Locate every malaria parasite.
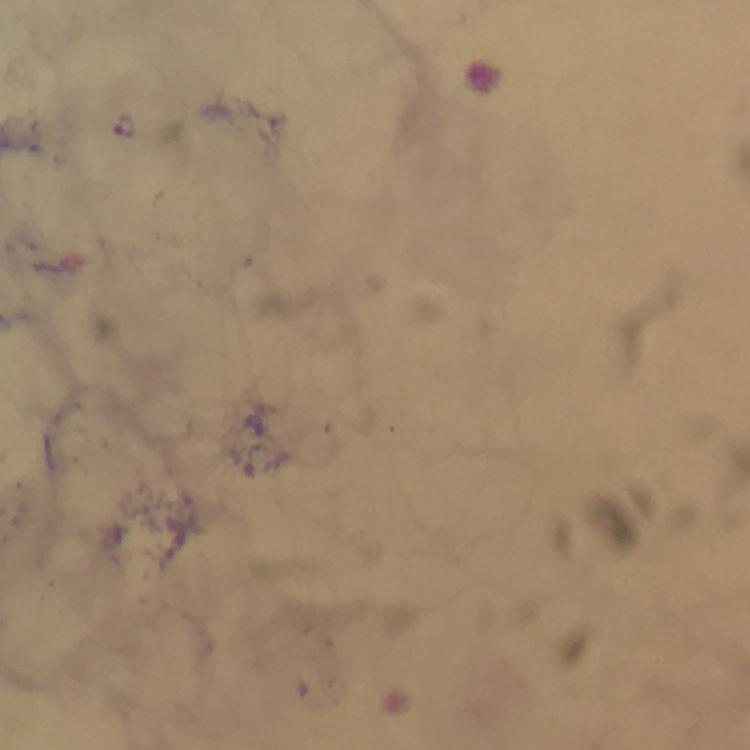

Approximate centers as (x, y) in pixels.
Malaria parasites: (125, 127).

Summary:
  - Context: from a diagnostic examination for malaria
  - Image size: 750×750 pixels
  - Magnification: 100x
  - Immersion oil: used
  - Stain: Giemsa
  - Capture: smartphone camera through the microscope
  - Preparation: thick smear
  - Cropped from: one field of view